Identify the cell.
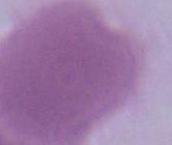

An erythrocyte.

Summary:
  - Magnification: 1000x
  - Modality: photomicrograph